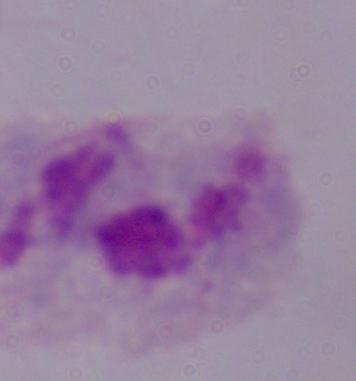 1000x magnification. Photomicrograph. A trichomonad is shown.